Locate and identify every blood parasite.
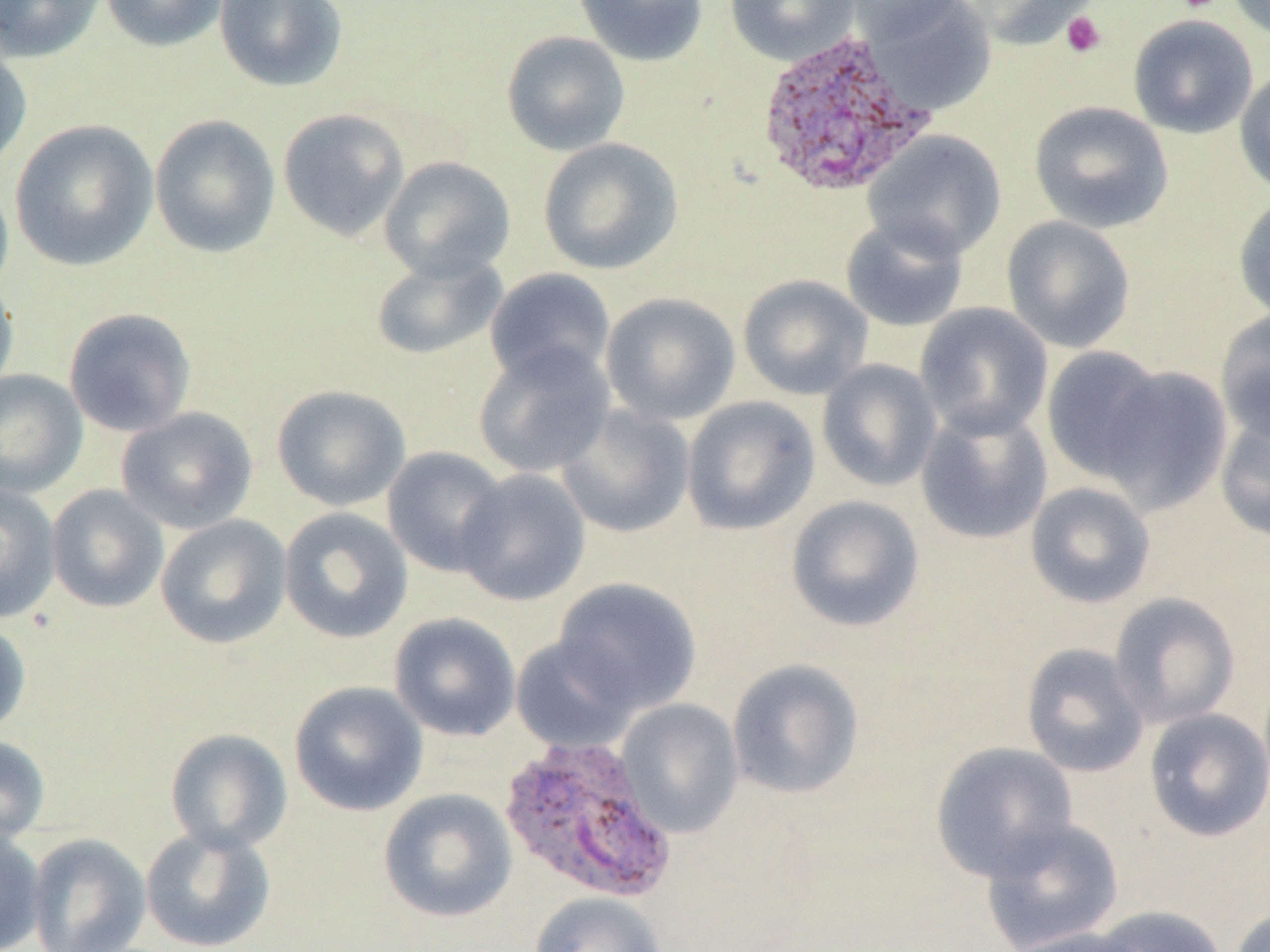
Approximate bounding boxes as (x1, y1, x2, y2) in pixels.
Plasmodium vivax-infected red blood cells: (753, 27, 937, 199), (497, 735, 678, 904).
No Plasmodium falciparum, Plasmodium ovale, Plasmodium malariae, Babesia divergens, or Trypanosoma brucei observed.

Summary:
  - Uninfected red blood cell locations: (0, 0, 105, 63), (100, 0, 229, 52), (214, 0, 348, 92), (573, 0, 709, 67), (725, 0, 860, 66), (845, 0, 967, 41), (862, 0, 998, 115), (965, 0, 1098, 50), (1227, 1, 1269, 42), (1128, 14, 1258, 139), (502, 31, 631, 156), (0, 39, 33, 173), (1234, 66, 1270, 196), (1029, 101, 1174, 234), (277, 108, 410, 241), (149, 114, 281, 258), (9, 119, 158, 272), (862, 130, 1007, 260), (538, 137, 683, 275), (379, 156, 515, 282), (0, 173, 14, 304), (1233, 194, 1270, 323), (840, 215, 969, 332), (1001, 215, 1136, 353), (370, 253, 507, 361), (484, 268, 616, 386), (0, 274, 19, 400), (737, 274, 873, 400), (599, 292, 741, 426), (915, 303, 1053, 441), (63, 307, 197, 438), (1215, 310, 1270, 446), (471, 340, 616, 478), (1040, 346, 1168, 484), (816, 359, 942, 492), (1094, 364, 1233, 514), (0, 369, 88, 498), (272, 384, 411, 511), (681, 395, 821, 535), (556, 404, 696, 538), (915, 405, 1053, 545), (116, 407, 258, 534), (1214, 412, 1270, 543), (382, 446, 511, 577), (454, 468, 591, 606), (1024, 481, 1156, 609), (0, 482, 61, 624), (46, 485, 169, 613), (785, 495, 925, 632), (279, 507, 413, 643), (155, 515, 292, 649), (553, 578, 702, 714), (1109, 592, 1240, 730), (389, 612, 521, 742), (0, 620, 31, 739), (510, 635, 640, 754), (1020, 642, 1149, 778), (727, 658, 865, 799), (289, 681, 428, 817), (615, 698, 744, 838), (1143, 707, 1270, 842), (165, 728, 293, 854), (0, 735, 51, 846), (930, 741, 1078, 881), (378, 788, 518, 922), (980, 816, 1125, 952), (140, 825, 277, 951), (0, 829, 46, 952), (26, 833, 151, 952), (528, 891, 668, 952), (1093, 905, 1229, 952), (1229, 905, 1269, 952), (1004, 924, 1152, 952)
  - Platelet locations: (1177, 0, 1221, 13), (1060, 11, 1107, 58)
  - Slide-level diagnosis: Plasmodium vivax
  - Modality: optical microscopy
  - Preparation: thin blood smear
  - Magnification: 1000x
  - Image size: 1270×952 pixels
  - Field of view: one of a larger specimen